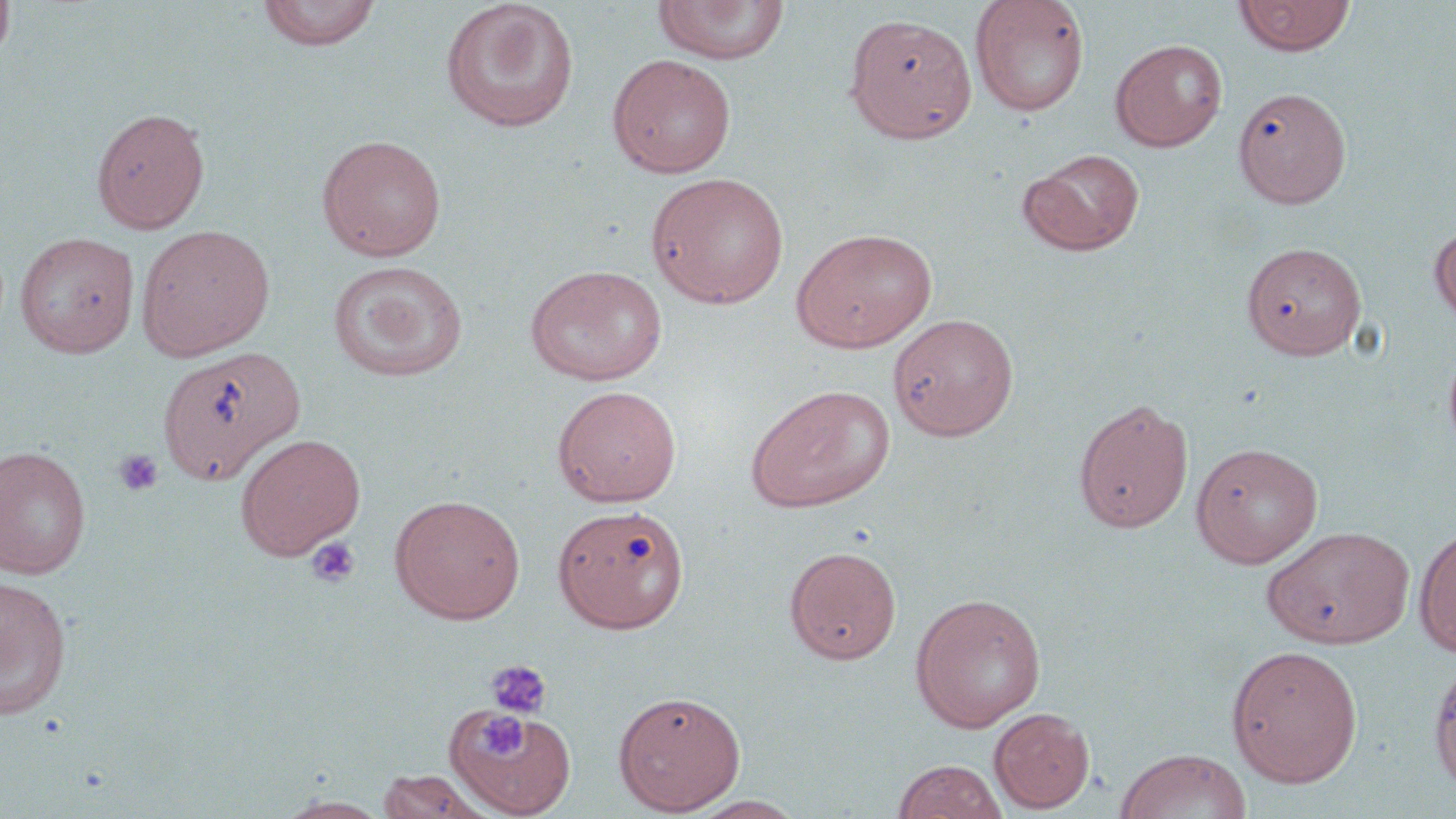
{
  "slide_level_diagnosis": "negative for blood parasites",
  "uninfected_red_blood_cell_locations": "approximate bounding boxes as (x1,y1)-(x2,y2) corner pairs in pixels: (0,0)-(16,64), (256,0)-(382,52), (969,0)-(1090,118), (1233,0)-(1355,56), (439,1)-(580,133), (653,1)-(790,65), (843,12)-(978,144), (1110,39)-(1228,151), (607,53)-(737,178), (1233,87)-(1350,208), (91,106)-(210,233), (316,134)-(447,261), (1020,148)-(1146,256), (646,172)-(791,309), (1430,224)-(1456,331), (136,225)-(275,361), (790,227)-(938,352), (14,232)-(140,358), (1247,244)-(1372,362), (327,261)-(469,382), (524,264)-(667,387), (887,313)-(1020,441), (1443,340)-(1456,464), (158,346)-(307,486), (745,384)-(896,513), (552,385)-(682,507), (1073,398)-(1194,533), (235,433)-(366,560), (1190,441)-(1323,568), (0,445)-(91,579), (389,494)-(526,624), (557,508)-(695,638), (1262,525)-(1416,649), (1414,525)-(1456,657), (784,545)-(902,664), (0,575)-(73,721), (909,592)-(1046,732), (1225,644)-(1363,787), (1428,656)-(1456,794), (612,690)-(747,815), (447,706)-(576,818), (989,708)-(1095,813), (1114,748)-(1252,819), (892,759)-(1009,819), (376,769)-(493,819), (683,795)-(809,818), (277,796)-(392,818)",
  "field_of_view": "one of a larger specimen",
  "preparation": "thin blood smear",
  "modality": "light microscopy",
  "stain": "May-Grünwald-Giemsa",
  "image_size": "1456×819 pixels",
  "magnification": "1000x",
  "platelet_locations": "approximate bounding boxes as (x1,y1)-(x2,y2) corner pairs in pixels: (113,448)-(163,497), (305,536)-(362,588), (485,659)-(552,719), (479,716)-(522,760)"
}